State the blood parasite species.
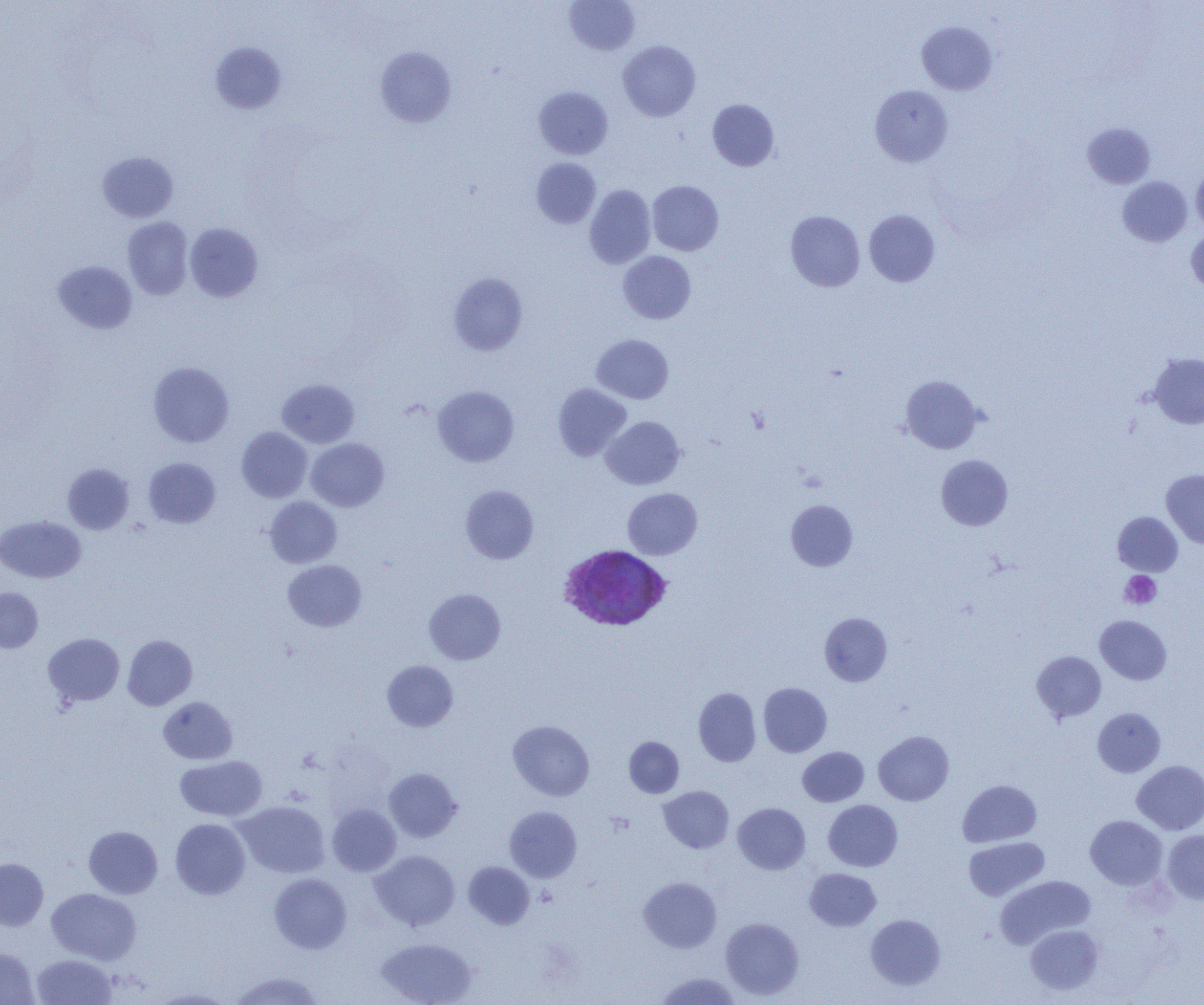
Plasmodium vivax.

Summary:
  - Coordinate format: approximate bounding boxes as named x1/y1/x2/y2 corners in pixels
  - Uninfected red blood cell locations: (x1=564, y1=0, x2=639, y2=56), (x1=917, y1=21, x2=997, y2=95), (x1=618, y1=40, x2=700, y2=121), (x1=209, y1=42, x2=287, y2=115), (x1=375, y1=47, x2=456, y2=127), (x1=870, y1=85, x2=953, y2=166), (x1=533, y1=87, x2=613, y2=159), (x1=707, y1=99, x2=779, y2=171), (x1=1082, y1=122, x2=1156, y2=189), (x1=97, y1=151, x2=178, y2=222), (x1=531, y1=157, x2=601, y2=228), (x1=1191, y1=164, x2=1204, y2=235), (x1=1117, y1=176, x2=1193, y2=247), (x1=647, y1=180, x2=724, y2=256), (x1=584, y1=185, x2=656, y2=268), (x1=785, y1=210, x2=865, y2=292), (x1=864, y1=210, x2=939, y2=287), (x1=122, y1=216, x2=193, y2=299), (x1=185, y1=223, x2=263, y2=302), (x1=1186, y1=228, x2=1204, y2=292), (x1=618, y1=251, x2=696, y2=324), (x1=52, y1=260, x2=138, y2=333), (x1=448, y1=272, x2=528, y2=355), (x1=591, y1=334, x2=674, y2=403), (x1=1148, y1=353, x2=1204, y2=429), (x1=148, y1=361, x2=234, y2=447), (x1=900, y1=375, x2=983, y2=454), (x1=277, y1=379, x2=359, y2=448), (x1=553, y1=383, x2=632, y2=461), (x1=433, y1=386, x2=519, y2=466), (x1=601, y1=416, x2=684, y2=490), (x1=236, y1=427, x2=312, y2=502), (x1=306, y1=438, x2=389, y2=511), (x1=936, y1=455, x2=1013, y2=530), (x1=144, y1=457, x2=220, y2=528), (x1=63, y1=463, x2=134, y2=534), (x1=1161, y1=469, x2=1204, y2=548), (x1=461, y1=485, x2=539, y2=563), (x1=1129, y1=487, x2=1202, y2=567), (x1=623, y1=488, x2=702, y2=559), (x1=264, y1=496, x2=342, y2=568), (x1=785, y1=499, x2=858, y2=571), (x1=1113, y1=512, x2=1183, y2=576), (x1=0, y1=515, x2=86, y2=582), (x1=283, y1=560, x2=366, y2=631), (x1=0, y1=587, x2=43, y2=653), (x1=424, y1=589, x2=505, y2=664), (x1=819, y1=612, x2=892, y2=686), (x1=1095, y1=615, x2=1172, y2=684), (x1=43, y1=633, x2=124, y2=706), (x1=122, y1=634, x2=197, y2=710), (x1=1032, y1=651, x2=1106, y2=722), (x1=382, y1=660, x2=458, y2=731), (x1=758, y1=682, x2=832, y2=757), (x1=693, y1=687, x2=761, y2=766), (x1=158, y1=697, x2=237, y2=764), (x1=1092, y1=708, x2=1166, y2=777), (x1=508, y1=720, x2=594, y2=801), (x1=873, y1=731, x2=954, y2=805), (x1=624, y1=737, x2=684, y2=798), (x1=798, y1=747, x2=868, y2=806), (x1=175, y1=756, x2=267, y2=821), (x1=1132, y1=760, x2=1204, y2=834), (x1=384, y1=768, x2=461, y2=842), (x1=958, y1=779, x2=1042, y2=847), (x1=659, y1=786, x2=733, y2=853), (x1=823, y1=800, x2=902, y2=871), (x1=235, y1=801, x2=330, y2=878), (x1=733, y1=803, x2=810, y2=874), (x1=327, y1=804, x2=401, y2=876), (x1=504, y1=806, x2=582, y2=882), (x1=1085, y1=815, x2=1167, y2=889), (x1=170, y1=818, x2=250, y2=899), (x1=84, y1=826, x2=162, y2=898), (x1=1161, y1=830, x2=1204, y2=904), (x1=963, y1=837, x2=1049, y2=901), (x1=370, y1=850, x2=460, y2=931), (x1=0, y1=858, x2=48, y2=930), (x1=463, y1=862, x2=535, y2=929), (x1=805, y1=868, x2=881, y2=930), (x1=269, y1=873, x2=351, y2=953), (x1=995, y1=875, x2=1096, y2=948), (x1=639, y1=877, x2=721, y2=952), (x1=47, y1=888, x2=141, y2=964), (x1=866, y1=914, x2=945, y2=989), (x1=721, y1=917, x2=804, y2=1000), (x1=1025, y1=924, x2=1104, y2=995), (x1=376, y1=937, x2=477, y2=1005), (x1=0, y1=948, x2=39, y2=1005), (x1=31, y1=954, x2=116, y2=1004), (x1=229, y1=971, x2=326, y2=1004), (x1=655, y1=972, x2=742, y2=1004), (x1=150, y1=988, x2=236, y2=1004)
  - Platelet locations: (x1=1120, y1=571, x2=1161, y2=608)
  - Plasmodium vivax-infected red blood cell locations: (x1=557, y1=544, x2=672, y2=631)
  - Image size: 1204×1005 pixels
  - Modality: light microscopy
  - Magnification: 1000x
  - Preparation: thin blood film
  - Field of view: one of a larger specimen